Report the malaria status of this cell.
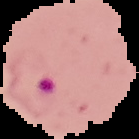
Parasitized.

Summary:
  - Image size: 139×139 pixels
  - Preparation: thin blood film
  - Image type: cell region segmented out of the field of view; surrounding area masked to black